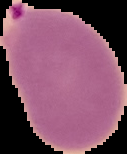 Malaria status: parasitized. From a thin blood smear. Cell region segmented out of the field of view; the surrounding area is masked to black. Image is 127×154 pixels.